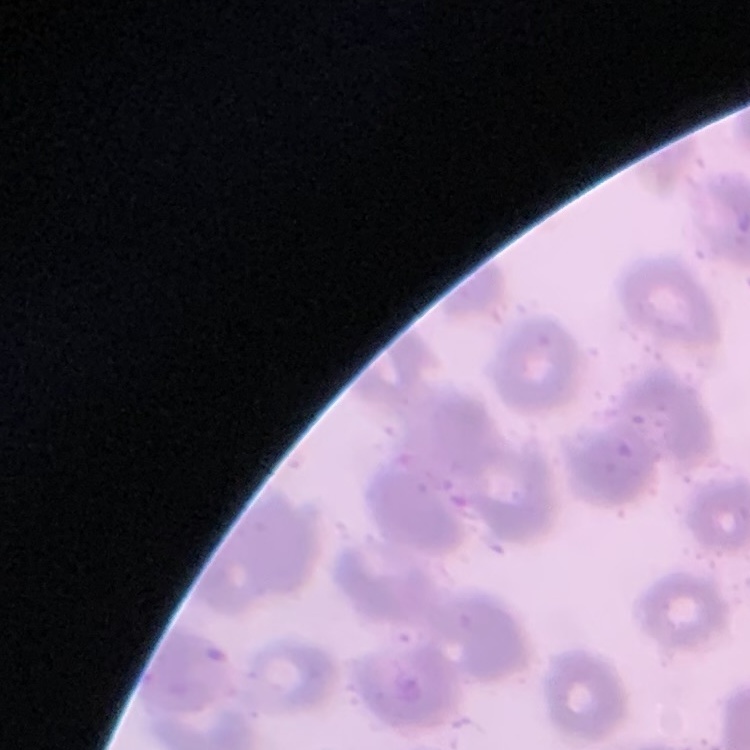

The erythrocytes show no rouleaux formation. Square crop of a larger photomicrograph. Thin blood film. Stained with either Field's or Giemsa.